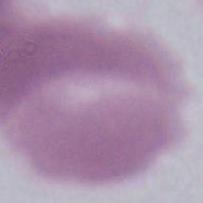

An erythrocyte is seen. Captured at 1000x magnification. Photomicrograph.